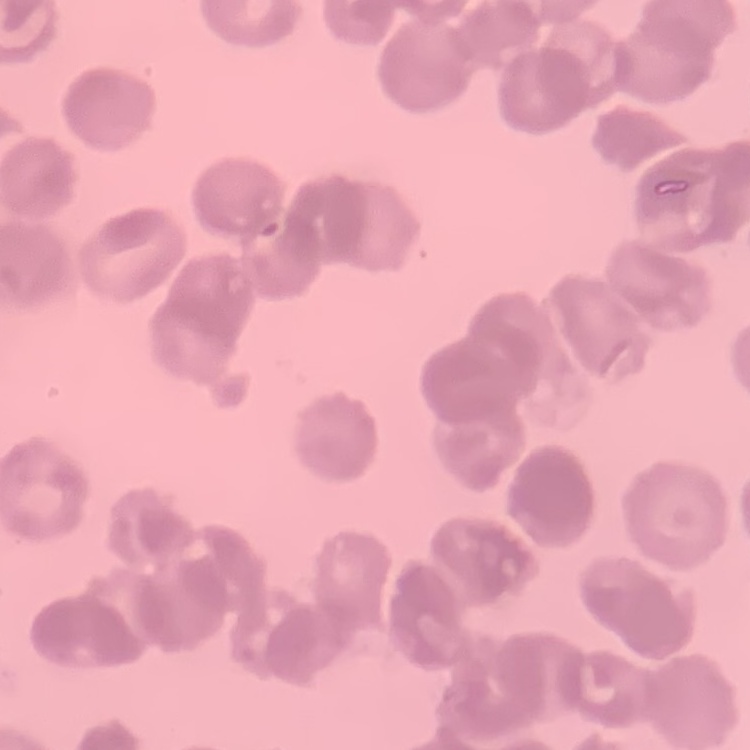
The red blood cells exhibit rouleaux formation. One tile cut from a larger photomicrograph. Thin peripheral smear. Field's or Giemsa stain.